Assess this cell for malaria.
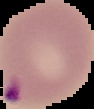
It is parasitized.

{
  "preparation": "thin blood smear",
  "image_size": "94×109 pixels",
  "image_type": "segmented cell region on a black background"
}